Report the malaria status of this cell.
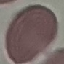
It is uninfected.

{
  "stain": "Giemsa",
  "capture": "smartphone camera at the microscope eyepiece",
  "image_type": "cell patch, automatically extracted from a larger field of view and resized to 64 × 64 pixels",
  "preparation": "thin blood smear"
}